Mark where platelets are.
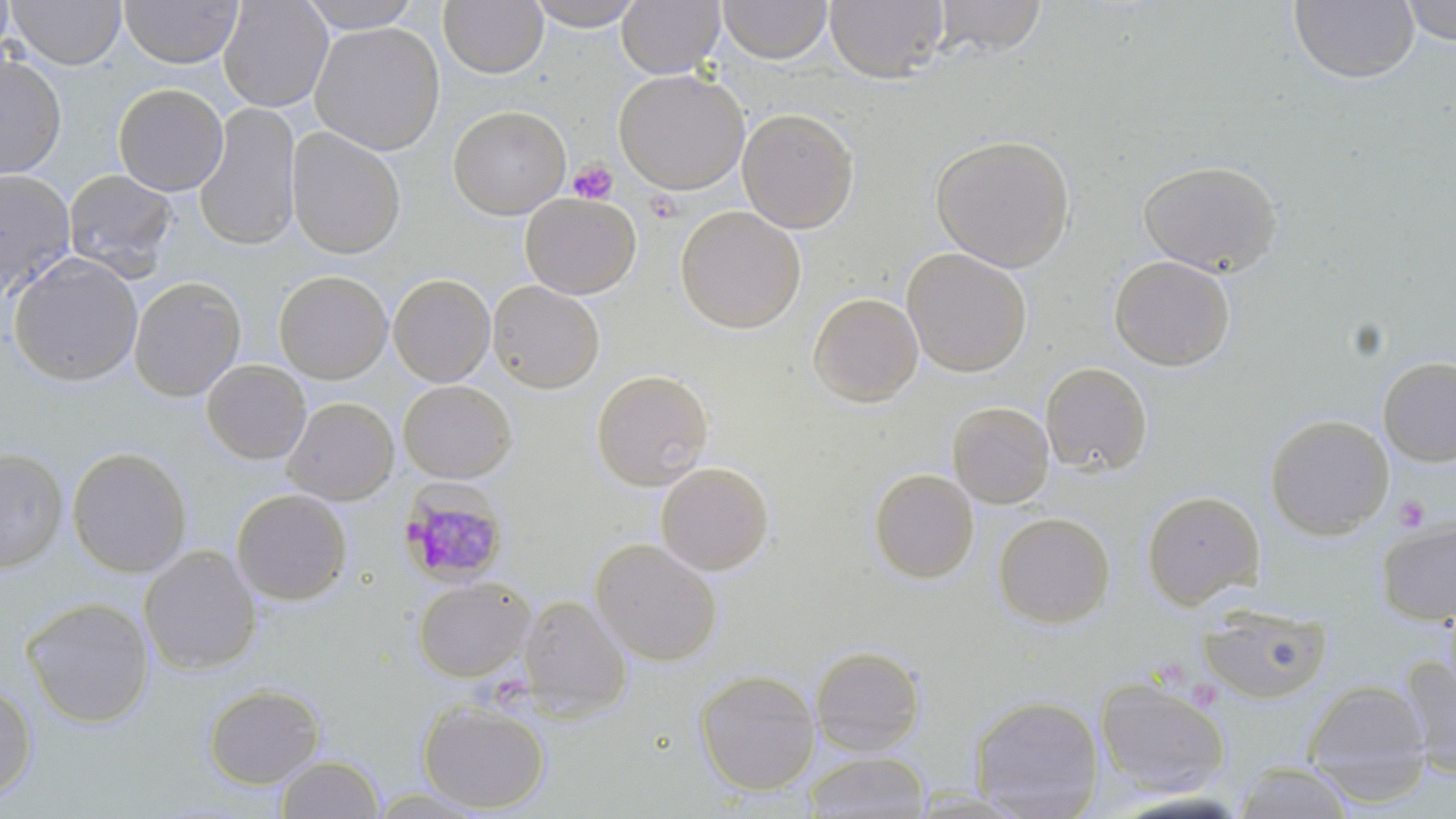
Approximate bounding boxes as named x1/y1/x2/y2 corners in pixels.
Platelets: (x1=568, y1=160, x2=618, y2=205), (x1=1393, y1=495, x2=1431, y2=532).

Summary:
  - Plasmodium malariae-infected red blood cell locations: (x1=398, y1=478, x2=507, y2=597)
  - Uninfected red blood cell locations: (x1=0, y1=0, x2=15, y2=62), (x1=7, y1=0, x2=126, y2=70), (x1=119, y1=0, x2=243, y2=68), (x1=217, y1=0, x2=333, y2=112), (x1=526, y1=0, x2=646, y2=30), (x1=617, y1=0, x2=725, y2=78), (x1=718, y1=0, x2=831, y2=64), (x1=824, y1=0, x2=948, y2=83), (x1=931, y1=0, x2=1048, y2=57), (x1=1400, y1=0, x2=1456, y2=46), (x1=297, y1=1, x2=425, y2=33), (x1=438, y1=1, x2=548, y2=79), (x1=1288, y1=1, x2=1420, y2=85), (x1=309, y1=21, x2=445, y2=156), (x1=0, y1=53, x2=66, y2=180), (x1=614, y1=69, x2=749, y2=195), (x1=113, y1=83, x2=229, y2=196), (x1=194, y1=102, x2=301, y2=251), (x1=448, y1=105, x2=571, y2=219), (x1=737, y1=108, x2=858, y2=234), (x1=285, y1=126, x2=406, y2=259), (x1=930, y1=134, x2=1076, y2=272), (x1=1138, y1=160, x2=1283, y2=277), (x1=63, y1=168, x2=178, y2=280), (x1=0, y1=170, x2=77, y2=295), (x1=520, y1=193, x2=641, y2=299), (x1=676, y1=205, x2=806, y2=333), (x1=901, y1=247, x2=1032, y2=378), (x1=8, y1=253, x2=143, y2=386), (x1=1108, y1=255, x2=1235, y2=372), (x1=274, y1=270, x2=392, y2=383), (x1=388, y1=274, x2=495, y2=387), (x1=128, y1=277, x2=246, y2=401), (x1=489, y1=280, x2=604, y2=393), (x1=807, y1=293, x2=924, y2=408), (x1=1378, y1=356, x2=1456, y2=467), (x1=201, y1=360, x2=311, y2=465), (x1=1040, y1=362, x2=1152, y2=477), (x1=591, y1=369, x2=714, y2=490), (x1=398, y1=380, x2=517, y2=483), (x1=282, y1=397, x2=398, y2=505), (x1=947, y1=401, x2=1054, y2=508), (x1=1264, y1=414, x2=1394, y2=540), (x1=66, y1=447, x2=193, y2=578), (x1=0, y1=448, x2=68, y2=573), (x1=655, y1=461, x2=774, y2=576), (x1=868, y1=469, x2=980, y2=584), (x1=231, y1=489, x2=352, y2=606), (x1=1141, y1=490, x2=1264, y2=609), (x1=993, y1=512, x2=1115, y2=629), (x1=1376, y1=515, x2=1456, y2=627), (x1=589, y1=538, x2=723, y2=667), (x1=138, y1=545, x2=261, y2=677), (x1=412, y1=578, x2=535, y2=682), (x1=519, y1=594, x2=633, y2=721), (x1=21, y1=597, x2=155, y2=728), (x1=1198, y1=603, x2=1332, y2=704), (x1=810, y1=645, x2=926, y2=758), (x1=1400, y1=655, x2=1456, y2=780), (x1=695, y1=669, x2=821, y2=796), (x1=1095, y1=675, x2=1231, y2=798), (x1=1303, y1=679, x2=1432, y2=805), (x1=0, y1=680, x2=37, y2=801), (x1=203, y1=683, x2=325, y2=790), (x1=970, y1=695, x2=1104, y2=818), (x1=418, y1=700, x2=550, y2=814), (x1=802, y1=751, x2=931, y2=818), (x1=275, y1=755, x2=384, y2=818), (x1=1231, y1=761, x2=1356, y2=819), (x1=364, y1=786, x2=495, y2=817)
  - Slide-level diagnosis: Plasmodium malariae
  - Modality: light microscopy
  - Preparation: thin blood smear
  - Field of view: one of a larger specimen
  - Stain: May-Grünwald-Giemsa
  - Image size: 1456×819 pixels
  - Magnification: 1000x